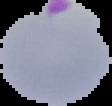
result = malaria parasites identified
image type = segmented cell region with the area outside set to black
image size = 112×106 pixels
preparation = thin blood film